Assess this cell for malaria.
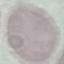

Uninfected.

Summary:
  - Image type: cell patch, automatically extracted from a larger field of view and resized to 64 × 64 pixels
  - Capture: smartphone camera at the microscope eyepiece
  - Preparation: thin blood film
  - Stain: Giemsa